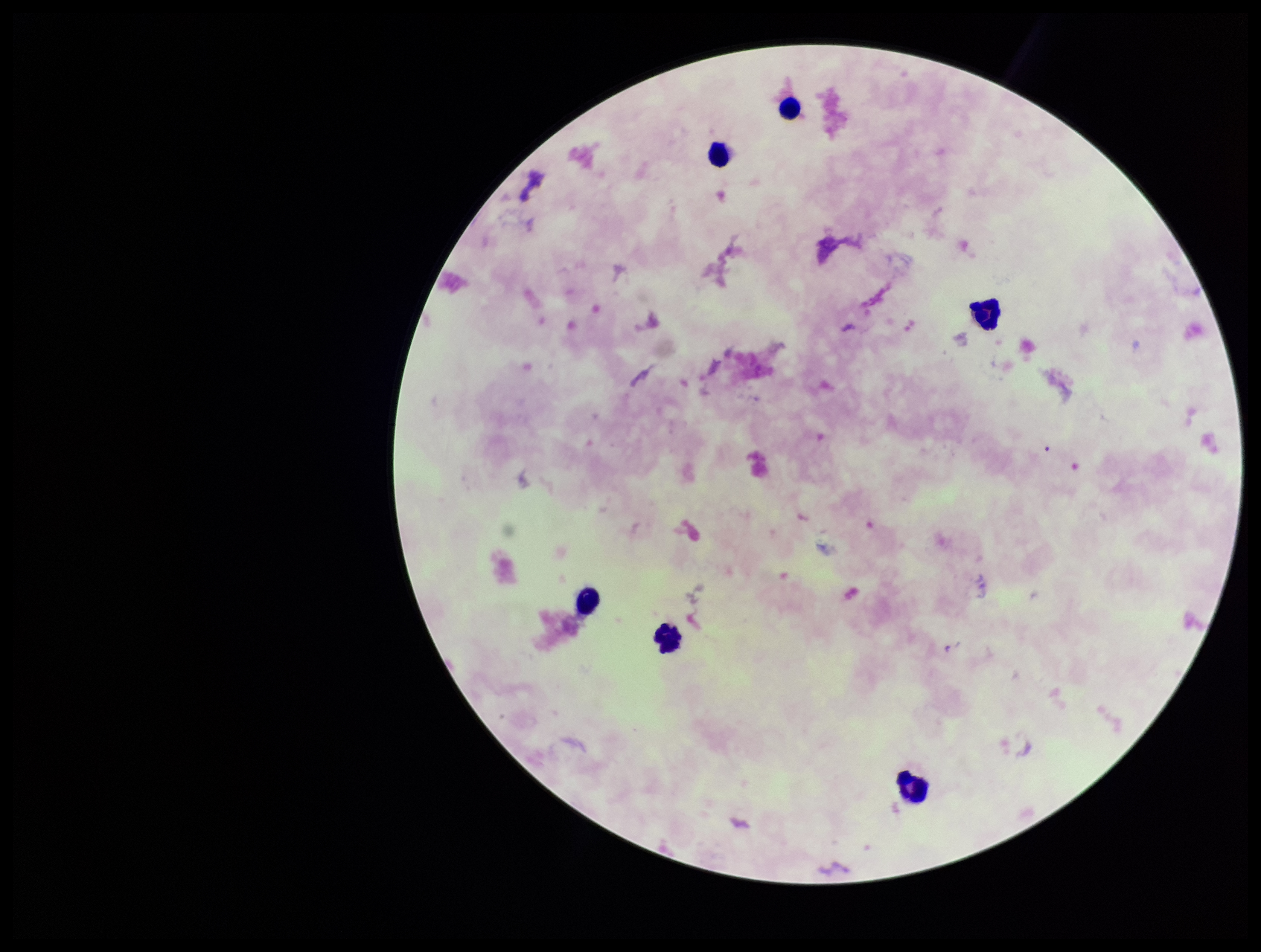

field of view = one from this slide
image size = 1261×952 pixels
parasite count = 0
Plasmodium parasites = none seen
patient malaria status = negative
capture = smartphone photograph through the microscope eyepiece
leukocyte count = 6
stain = Giemsa
preparation = thick smear